Name the blood parasite species.
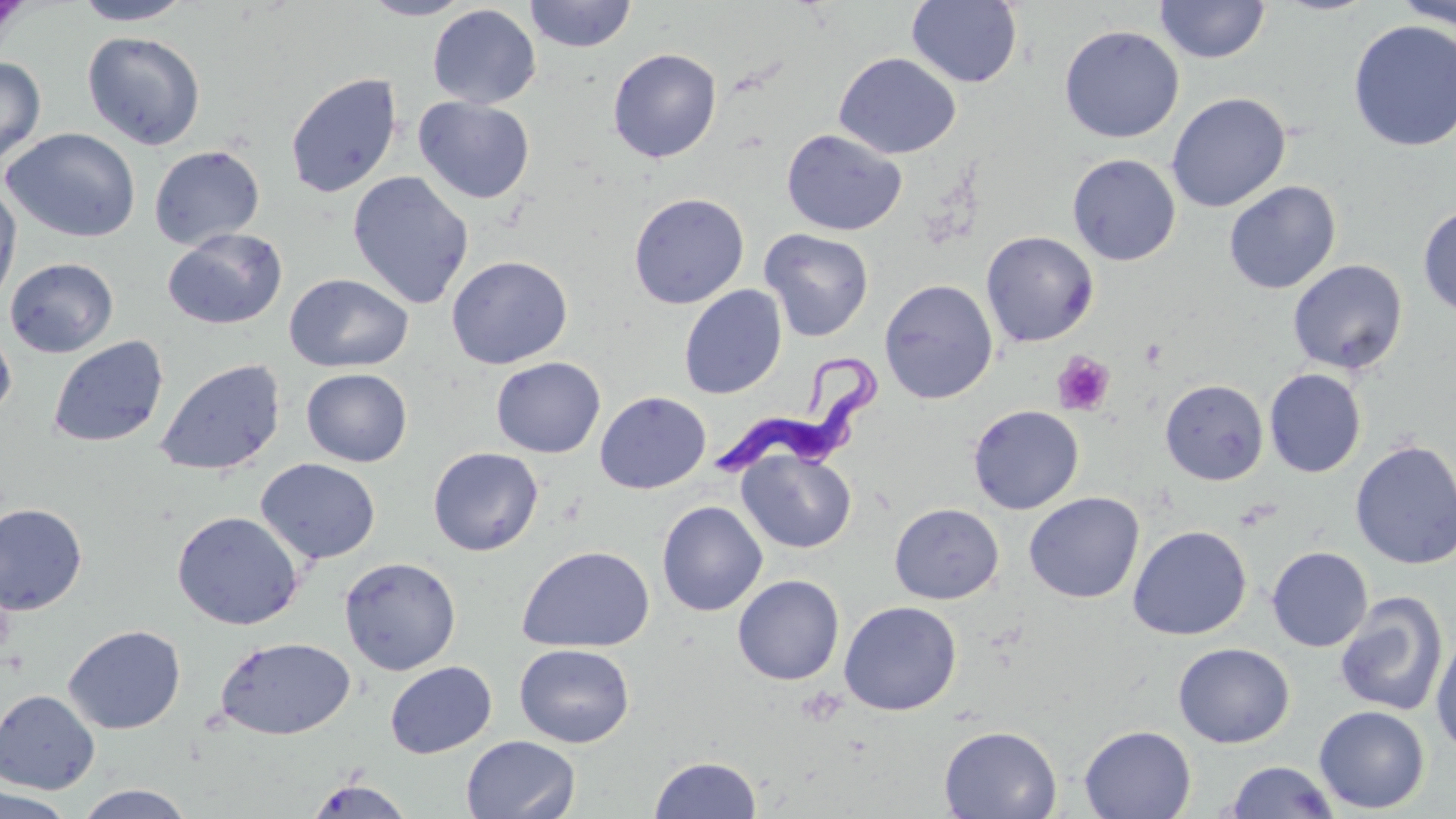
Trypanosoma brucei.

preparation = thin blood film
image size = 1456×819 pixels
platelet locations = approximate bounding boxes as named x1/y1/x2/y2 corners in pixels: (x1=1141, y1=339, x2=1167, y2=367), (x1=1052, y1=350, x2=1115, y2=415), (x1=799, y1=688, x2=844, y2=727)
magnification = 1000x
stain = May-Grünwald-Giemsa
Trypanosoma brucei locations = approximate bounding boxes as named x1/y1/x2/y2 corners in pixels: (x1=715, y1=352, x2=878, y2=478)
uninfected red blood cell locations = approximate bounding boxes as named x1/y1/x2/y2 corners in pixels: (x1=359, y1=0, x2=475, y2=20), (x1=524, y1=0, x2=637, y2=53), (x1=906, y1=0, x2=1023, y2=89), (x1=1155, y1=0, x2=1271, y2=64), (x1=1393, y1=0, x2=1455, y2=31), (x1=73, y1=1, x2=192, y2=25), (x1=427, y1=4, x2=541, y2=109), (x1=1347, y1=19, x2=1456, y2=152), (x1=1059, y1=24, x2=1184, y2=143), (x1=82, y1=31, x2=206, y2=150), (x1=607, y1=48, x2=722, y2=163), (x1=834, y1=52, x2=962, y2=159), (x1=0, y1=56, x2=46, y2=170), (x1=285, y1=72, x2=402, y2=199), (x1=1166, y1=92, x2=1291, y2=213), (x1=413, y1=96, x2=535, y2=204), (x1=2, y1=128, x2=141, y2=243), (x1=781, y1=129, x2=907, y2=236), (x1=149, y1=145, x2=265, y2=249), (x1=1067, y1=153, x2=1181, y2=266), (x1=348, y1=171, x2=474, y2=309), (x1=1223, y1=180, x2=1341, y2=294), (x1=0, y1=185, x2=22, y2=309), (x1=628, y1=192, x2=750, y2=309), (x1=1418, y1=202, x2=1456, y2=319), (x1=162, y1=228, x2=287, y2=331), (x1=758, y1=228, x2=875, y2=341), (x1=980, y1=230, x2=1099, y2=348), (x1=446, y1=255, x2=573, y2=369), (x1=4, y1=257, x2=118, y2=358), (x1=1287, y1=259, x2=1408, y2=375), (x1=284, y1=272, x2=413, y2=373), (x1=879, y1=278, x2=999, y2=404), (x1=678, y1=284, x2=788, y2=399), (x1=0, y1=320, x2=17, y2=418), (x1=48, y1=335, x2=169, y2=448), (x1=491, y1=356, x2=606, y2=458), (x1=154, y1=358, x2=287, y2=477), (x1=301, y1=368, x2=413, y2=467), (x1=1264, y1=368, x2=1366, y2=478), (x1=1160, y1=379, x2=1269, y2=485), (x1=595, y1=391, x2=710, y2=494), (x1=967, y1=405, x2=1084, y2=514), (x1=1350, y1=439, x2=1456, y2=570), (x1=427, y1=446, x2=544, y2=556), (x1=736, y1=448, x2=856, y2=554), (x1=255, y1=457, x2=381, y2=564), (x1=1024, y1=492, x2=1144, y2=604), (x1=657, y1=500, x2=768, y2=617), (x1=0, y1=502, x2=88, y2=615), (x1=889, y1=503, x2=1004, y2=604), (x1=171, y1=510, x2=304, y2=630), (x1=1127, y1=525, x2=1252, y2=640), (x1=516, y1=545, x2=655, y2=653), (x1=1267, y1=546, x2=1372, y2=652), (x1=339, y1=556, x2=462, y2=675), (x1=732, y1=574, x2=845, y2=685), (x1=1334, y1=591, x2=1449, y2=716), (x1=839, y1=600, x2=962, y2=716), (x1=63, y1=624, x2=186, y2=734), (x1=1431, y1=629, x2=1456, y2=756), (x1=215, y1=636, x2=356, y2=740), (x1=1173, y1=642, x2=1295, y2=748), (x1=514, y1=643, x2=635, y2=748), (x1=385, y1=661, x2=497, y2=758), (x1=0, y1=689, x2=100, y2=794), (x1=1314, y1=705, x2=1430, y2=814), (x1=938, y1=725, x2=1062, y2=818), (x1=1079, y1=725, x2=1196, y2=819), (x1=461, y1=735, x2=581, y2=818), (x1=648, y1=754, x2=762, y2=818), (x1=1224, y1=761, x2=1340, y2=818), (x1=304, y1=779, x2=415, y2=819), (x1=73, y1=784, x2=198, y2=818), (x1=0, y1=787, x2=77, y2=819)
modality = light microscopy
field of view = single